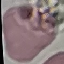

result: negative for malaria parasites
capture: smartphone camera at the microscope eyepiece
stain: Giemsa
image_type: automatically extracted cell patch, resized to 64 × 64 pixels
preparation: thin blood smear